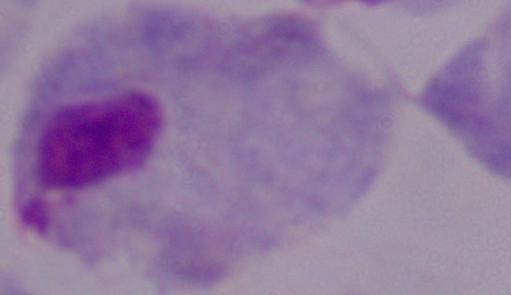
identification = trichomonad
magnification = 1000x
modality = photomicrograph